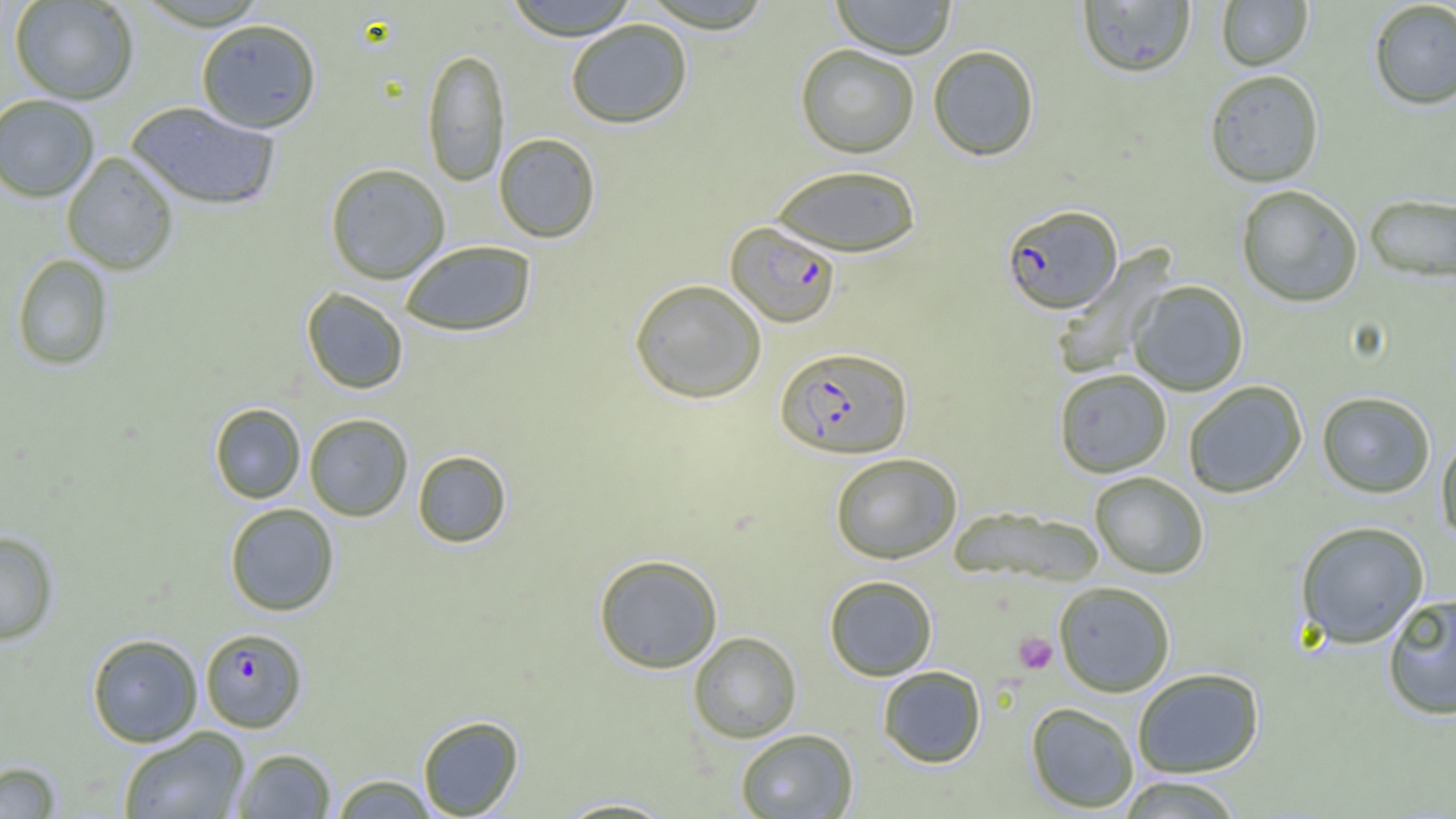

Approximate bounding boxes as (x1, y1, x2, y2) in pixels. Uninfected red blood cell locations: (9, 0, 139, 104), (504, 0, 638, 40), (638, 0, 776, 33), (831, 0, 957, 58), (1076, 1, 1197, 78), (1216, 1, 1313, 71), (1368, 1, 1456, 109), (195, 18, 322, 133), (565, 19, 693, 129), (795, 44, 919, 158), (927, 45, 1040, 161), (422, 47, 510, 186), (1204, 69, 1325, 188), (0, 94, 100, 202), (126, 101, 281, 211), (493, 133, 601, 243), (61, 152, 179, 275), (325, 163, 450, 284), (771, 164, 922, 257), (1236, 184, 1364, 307), (1364, 193, 1456, 283), (400, 240, 536, 336), (1052, 246, 1175, 379), (11, 253, 114, 371), (629, 278, 767, 403), (1129, 280, 1249, 396), (301, 287, 409, 394), (1054, 369, 1172, 477), (1183, 381, 1308, 498), (1316, 391, 1435, 498), (209, 403, 306, 503), (304, 413, 413, 521), (1435, 434, 1456, 544), (412, 450, 512, 547), (830, 452, 962, 563), (1089, 471, 1209, 579), (225, 503, 339, 616), (950, 507, 1105, 587), (1294, 520, 1430, 648), (0, 531, 59, 645), (593, 554, 723, 673), (824, 574, 938, 681), (1054, 581, 1176, 697), (1381, 594, 1456, 720), (688, 631, 802, 743), (87, 633, 203, 747), (877, 666, 986, 768), (1132, 668, 1265, 778), (1025, 702, 1139, 812), (417, 715, 524, 818), (118, 727, 250, 819), (735, 728, 858, 819), (232, 748, 336, 818), (0, 760, 62, 819), (329, 774, 438, 817), (1114, 775, 1246, 818), (553, 796, 678, 818). Platelet locations: (1014, 632, 1058, 674). Plasmodium falciparum-infected red blood cell locations: (1001, 203, 1123, 314), (726, 222, 841, 327), (776, 346, 912, 458), (200, 627, 307, 732). Slide-level diagnosis: Plasmodium falciparum. Captured at 1000x magnification. Image is 1456×819 pixels. One field of a larger specimen. Light microscopy. Thin blood smear.